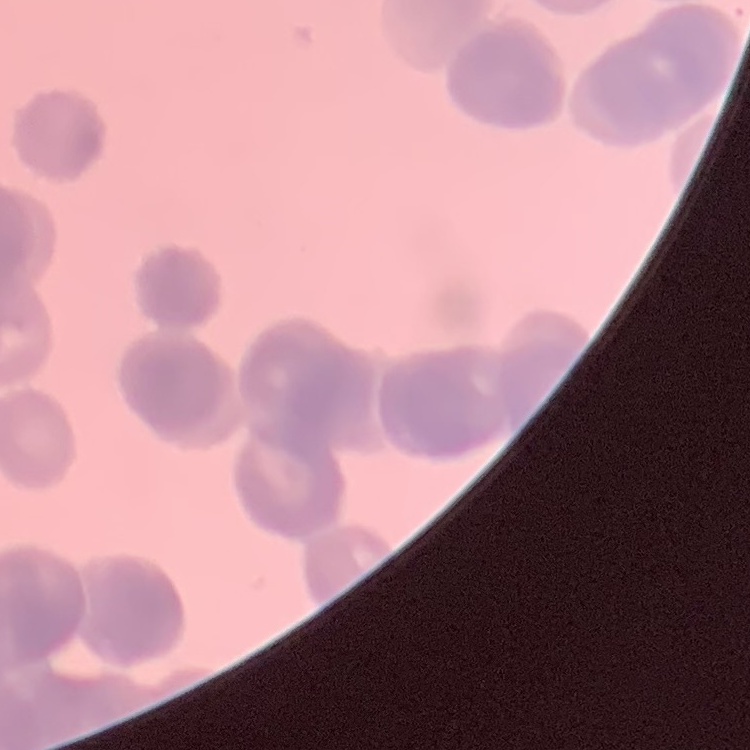

erythrocyte morphology = rouleaux formation
preparation = thin blood smear
stain = Field's or Giemsa
image type = one tile cut from a larger photomicrograph